Name the blood parasite species.
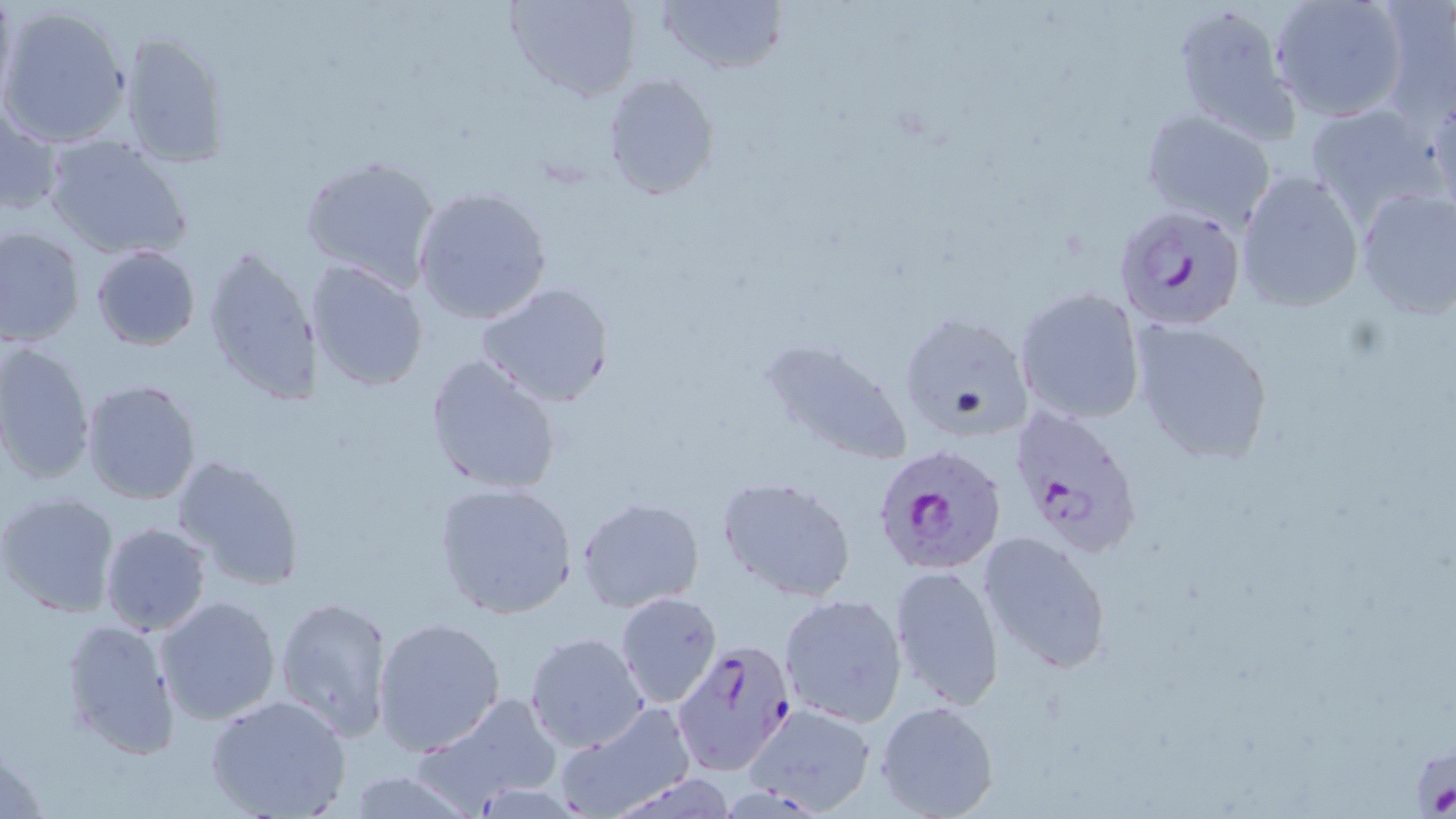
Plasmodium falciparum.

Summary:
  - Coordinate format: approximate bounding boxes as (x1,y1)-(x2,y2) corner pairs in pixels
  - Plasmodium falciparum-infected red blood cell locations: (1116,203)-(1249,333), (1006,405)-(1144,559), (872,445)-(1006,575), (671,639)-(795,774)
  - Uninfected red blood cell locations: (1,0)-(18,111), (504,0)-(640,101), (655,0)-(787,76), (1269,0)-(1410,122), (1171,1)-(1303,144), (1373,3)-(1455,128), (0,5)-(132,148), (116,30)-(231,170), (603,73)-(720,199), (1427,89)-(1455,218), (1,100)-(65,221), (1304,101)-(1448,225), (1139,110)-(1278,230), (43,133)-(192,260), (298,155)-(442,290), (1236,169)-(1364,311), (412,186)-(554,324), (1352,186)-(1456,320), (1,226)-(85,346), (202,242)-(325,407), (91,245)-(200,350), (306,260)-(429,393), (475,282)-(619,409), (1013,288)-(1146,425), (897,312)-(1034,443), (1129,318)-(1276,466), (0,341)-(96,485), (760,341)-(917,468), (425,353)-(563,497), (78,378)-(202,506), (171,454)-(306,591), (718,476)-(857,602), (433,481)-(580,621), (0,491)-(122,619), (577,497)-(705,612), (100,523)-(211,636), (976,530)-(1113,674), (888,563)-(1005,711), (615,592)-(722,707), (779,593)-(907,726), (153,595)-(281,725), (273,595)-(394,741), (60,615)-(182,761), (373,616)-(506,755), (524,631)-(650,753), (205,693)-(351,818), (420,694)-(561,812), (876,700)-(1001,819), (555,702)-(696,819), (738,702)-(880,816), (340,769)-(479,819)
  - Stain: May-Grünwald-Giemsa
  - Image size: 1456×819 pixels
  - Magnification: 1000x
  - Field of view: one of a larger specimen
  - Preparation: thin blood film
  - Modality: optical microscopy